Assess this cell for malaria.
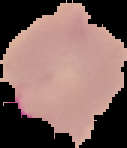

It is parasitized.

Cell region segmented out of the field of view; the surrounding area is masked to black. Image is 127×148 pixels. From a thin blood smear.